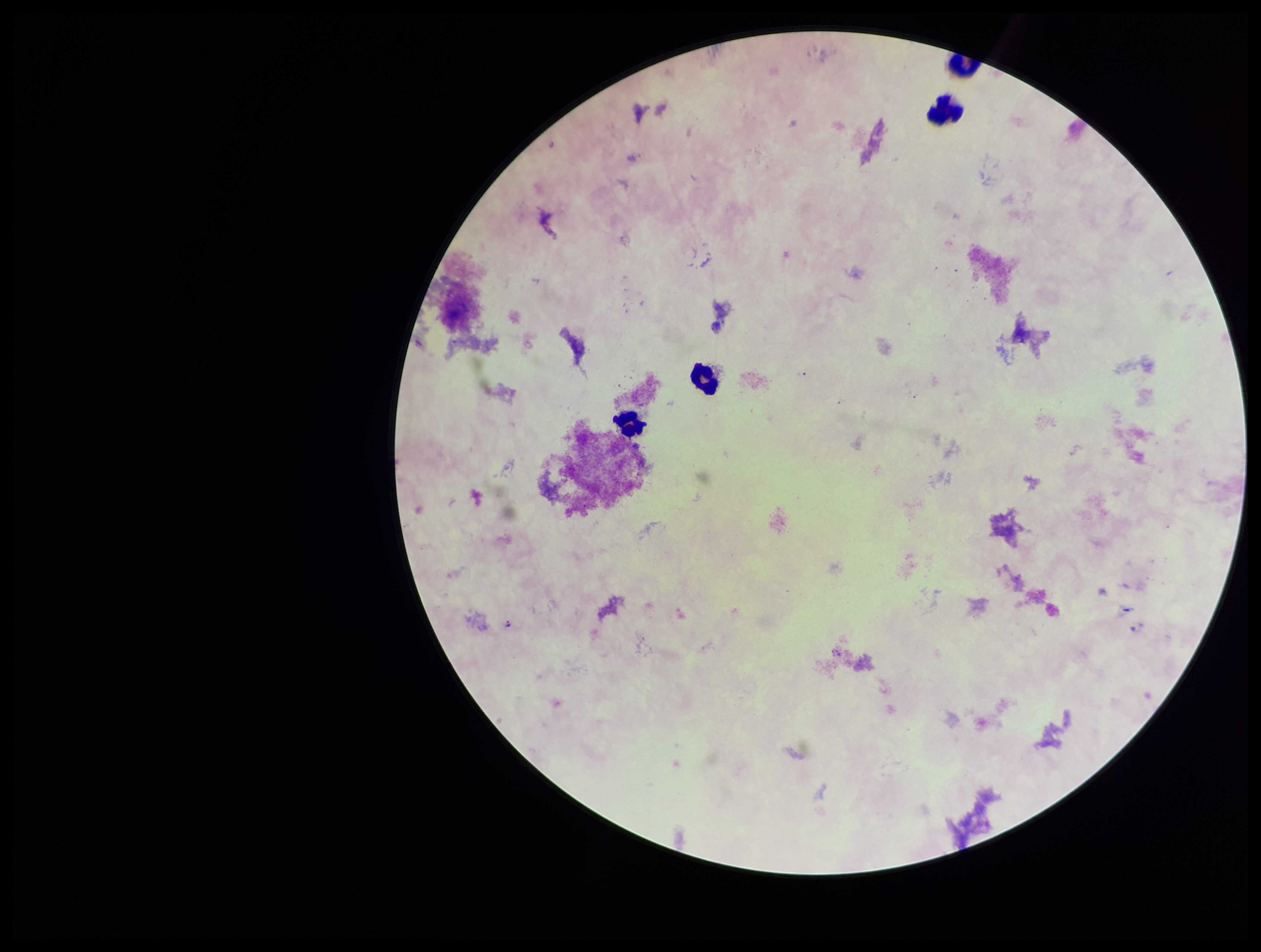

Summary:
  - Stain: Giemsa
  - Field of view: single
  - Preparation: thick smear
  - Image size: 1261×952 pixels
  - Leukocyte count: 4
  - Capture: smartphone photograph through the microscope eyepiece
  - Species reported for this patient: Plasmodium falciparum
  - Patient malaria status: positive
  - Parasite count: 0
  - Plasmodium parasites: none identified